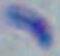

1000x magnification. Toxoplasma gondii is shown. Photomicrograph.